Classify this cell by malaria status.
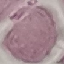

Uninfected.

Acquired by smartphone through the microscope eyepiece. Thin blood film. Automatically extracted cell patch, resized to 64 × 64 pixels. Giemsa stain.